Outline each blood parasite and name the species.
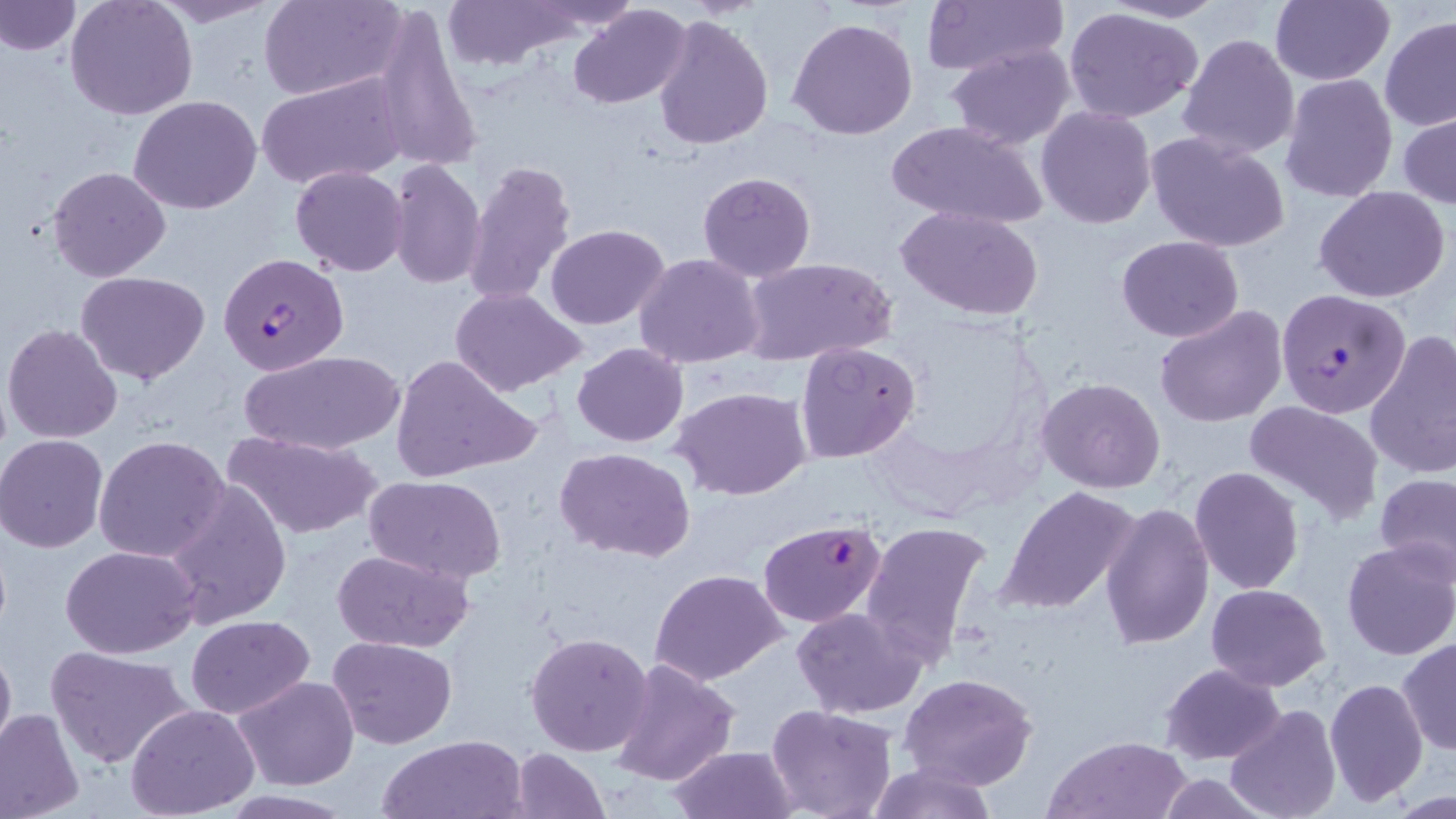
Approximate bounding boxes as named x1/y1/x2/y2 corners in pixels.
Plasmodium falciparum-infected red blood cells: (x1=218, y1=252, x2=350, y2=375), (x1=1275, y1=288, x2=1411, y2=417), (x1=757, y1=518, x2=889, y2=641).
No Plasmodium ovale, Plasmodium malariae, Plasmodium vivax, Babesia divergens, or Trypanosoma brucei observed.

Uninfected red blood cell locations: (x1=0, y1=0, x2=80, y2=56), (x1=144, y1=0, x2=281, y2=28), (x1=260, y1=0, x2=407, y2=101), (x1=441, y1=0, x2=580, y2=69), (x1=530, y1=0, x2=641, y2=31), (x1=918, y1=0, x2=1068, y2=78), (x1=1098, y1=0, x2=1229, y2=23), (x1=65, y1=1, x2=197, y2=121), (x1=1269, y1=1, x2=1395, y2=85), (x1=371, y1=5, x2=485, y2=176), (x1=568, y1=5, x2=690, y2=110), (x1=1061, y1=6, x2=1207, y2=126), (x1=652, y1=13, x2=774, y2=150), (x1=1381, y1=15, x2=1456, y2=132), (x1=788, y1=16, x2=919, y2=140), (x1=1177, y1=34, x2=1300, y2=161), (x1=945, y1=42, x2=1076, y2=148), (x1=256, y1=73, x2=409, y2=189), (x1=1281, y1=74, x2=1398, y2=203), (x1=129, y1=95, x2=262, y2=215), (x1=1036, y1=106, x2=1157, y2=228), (x1=1398, y1=109, x2=1456, y2=210), (x1=886, y1=120, x2=1050, y2=231), (x1=1146, y1=130, x2=1290, y2=252), (x1=385, y1=158, x2=487, y2=291), (x1=464, y1=160, x2=579, y2=309), (x1=290, y1=165, x2=410, y2=276), (x1=48, y1=166, x2=172, y2=282), (x1=697, y1=170, x2=816, y2=281), (x1=1314, y1=186, x2=1450, y2=303), (x1=897, y1=206, x2=1043, y2=319), (x1=545, y1=224, x2=669, y2=329), (x1=1116, y1=235, x2=1243, y2=343), (x1=635, y1=254, x2=766, y2=369), (x1=740, y1=257, x2=896, y2=367), (x1=75, y1=271, x2=211, y2=387), (x1=450, y1=287, x2=587, y2=395), (x1=1155, y1=304, x2=1288, y2=427), (x1=3, y1=322, x2=124, y2=444), (x1=1364, y1=328, x2=1456, y2=478), (x1=796, y1=340, x2=923, y2=463), (x1=572, y1=342, x2=689, y2=447), (x1=238, y1=349, x2=405, y2=458), (x1=390, y1=353, x2=541, y2=485), (x1=1036, y1=377, x2=1166, y2=492), (x1=670, y1=386, x2=812, y2=499), (x1=1244, y1=399, x2=1384, y2=523), (x1=224, y1=429, x2=381, y2=540), (x1=2, y1=434, x2=110, y2=553), (x1=94, y1=434, x2=229, y2=561), (x1=555, y1=447, x2=698, y2=565), (x1=1190, y1=466, x2=1304, y2=596), (x1=1375, y1=473, x2=1456, y2=581), (x1=363, y1=475, x2=507, y2=585), (x1=160, y1=478, x2=292, y2=627), (x1=997, y1=486, x2=1141, y2=615), (x1=1100, y1=502, x2=1214, y2=652), (x1=860, y1=519, x2=996, y2=664), (x1=1339, y1=538, x2=1456, y2=661), (x1=62, y1=545, x2=202, y2=657), (x1=331, y1=548, x2=478, y2=655), (x1=648, y1=567, x2=789, y2=684), (x1=1205, y1=584, x2=1331, y2=690), (x1=791, y1=606, x2=928, y2=718), (x1=186, y1=616, x2=314, y2=718), (x1=525, y1=630, x2=655, y2=758), (x1=0, y1=635, x2=15, y2=763), (x1=329, y1=635, x2=459, y2=748), (x1=1397, y1=638, x2=1455, y2=757), (x1=45, y1=644, x2=194, y2=769), (x1=611, y1=658, x2=741, y2=788), (x1=1159, y1=663, x2=1285, y2=764), (x1=898, y1=673, x2=1040, y2=791), (x1=234, y1=676, x2=361, y2=789), (x1=1324, y1=678, x2=1429, y2=806), (x1=765, y1=703, x2=900, y2=819), (x1=1225, y1=703, x2=1342, y2=819), (x1=126, y1=704, x2=259, y2=817), (x1=0, y1=707, x2=85, y2=819), (x1=377, y1=734, x2=527, y2=819), (x1=1044, y1=734, x2=1189, y2=818), (x1=666, y1=744, x2=801, y2=819), (x1=506, y1=747, x2=611, y2=819), (x1=863, y1=759, x2=997, y2=819). Slide-level diagnosis: Plasmodium falciparum. One field of a larger specimen. Thin blood film. Image is 1456×819 pixels. May-Grünwald-Giemsa-stained preparation. 1000x magnification. Light microscopy.